Assess the morphology of the red blood cells.
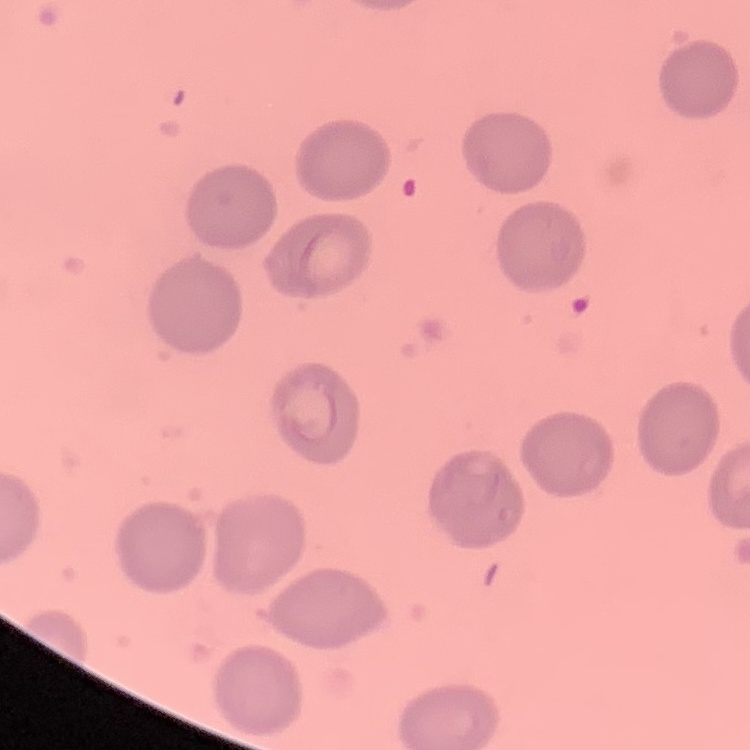

No rouleaux formation.

preparation: thin blood film
image_type: one tile cut from a larger photomicrograph
stain: Field's or Giemsa